Locate every malaria parasite.
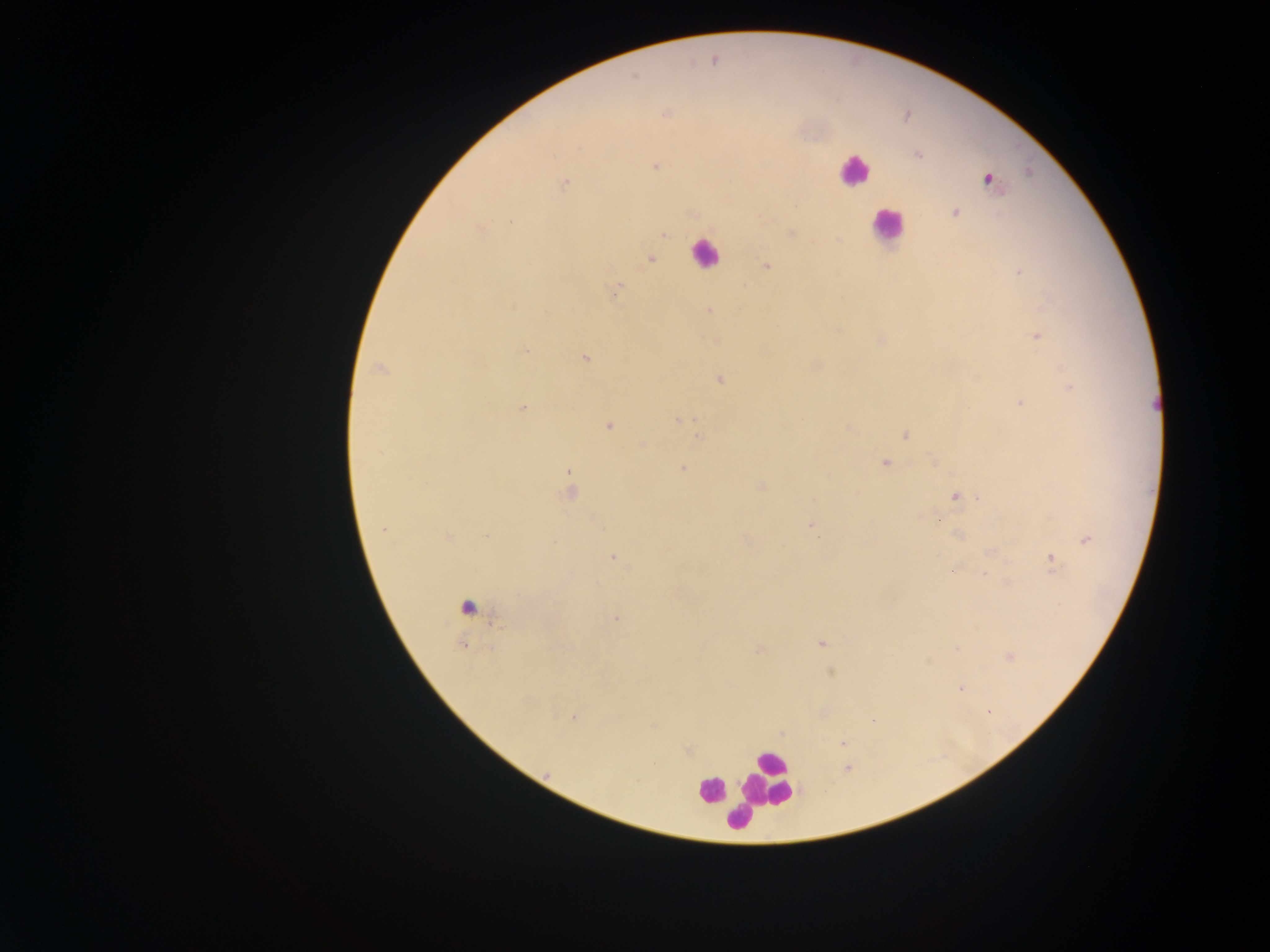
Approximate centers as {x, y} in pixels.
Malaria parasites: {713, 59}, {666, 113}, {917, 154}, {655, 167}, {986, 179}, {564, 183}, {954, 211}, {511, 222}, {791, 232}, {663, 233}, {650, 259}, {765, 266}, {1019, 273}, {616, 290}, {709, 311}, {1036, 336}, {881, 340}, {716, 341}, {526, 351}, {583, 358}, {816, 365}, {378, 369}, {719, 379}, {1070, 388}, {1020, 403}, {521, 407}, {678, 419}, {607, 425}, {847, 427}, {698, 435}, {906, 435}, {641, 444}, {884, 462}, {683, 468}, {569, 474}, {760, 486}, {570, 490}, {956, 496}, {980, 498}, {937, 519}, {811, 525}, {958, 534}, {447, 536}, {1086, 540}, {993, 551}, {614, 556}, {1050, 559}, {957, 566}, {985, 574}, {1006, 583}, {616, 618}, {820, 643}, {463, 645}, {758, 650}, {1009, 656}, {830, 672}, {961, 688}, {822, 712}, {574, 717}, {873, 721}, {653, 726}, {843, 743}, {687, 750}, {846, 768}.

preparation = thick blood smear
leukocyte locations = approximate centers as {x, y} in pixels: {853, 170}, {886, 225}, {704, 253}, {466, 606}, {766, 781}, {711, 789}, {727, 801}, {744, 808}, {739, 817}
field of view = single
capture = mobile-phone photograph through a microscope
country = Ghana
image size = 1270×952 pixels